Point out each Plasmodium parasite.
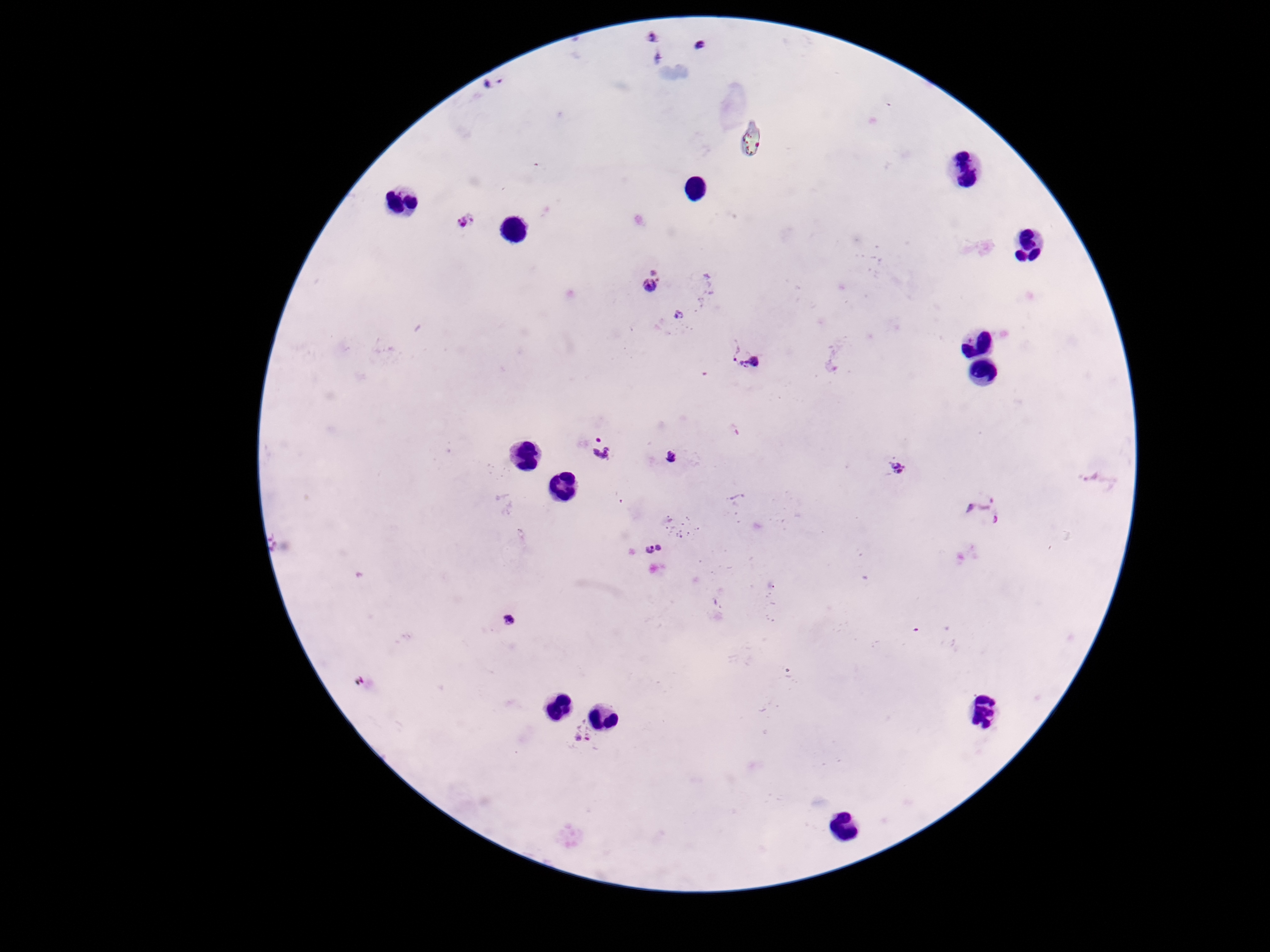

Approximate centers as [x, y] in pixels.
Plasmodium parasites: [651, 40], [700, 46], [494, 84], [467, 223], [652, 283], [678, 318], [747, 358], [598, 449], [671, 456], [896, 468], [1095, 479], [984, 510], [654, 551], [510, 620], [580, 733].

magnification: 100x
preparation: thick blood film
capture: smartphone camera through the microscope eyepiece
image_size: 1270×952 pixels
patient_malaria_status: infected
stain: Giemsa
field_of_view: single